Locate every Plasmodium malariae-infected red blood cell.
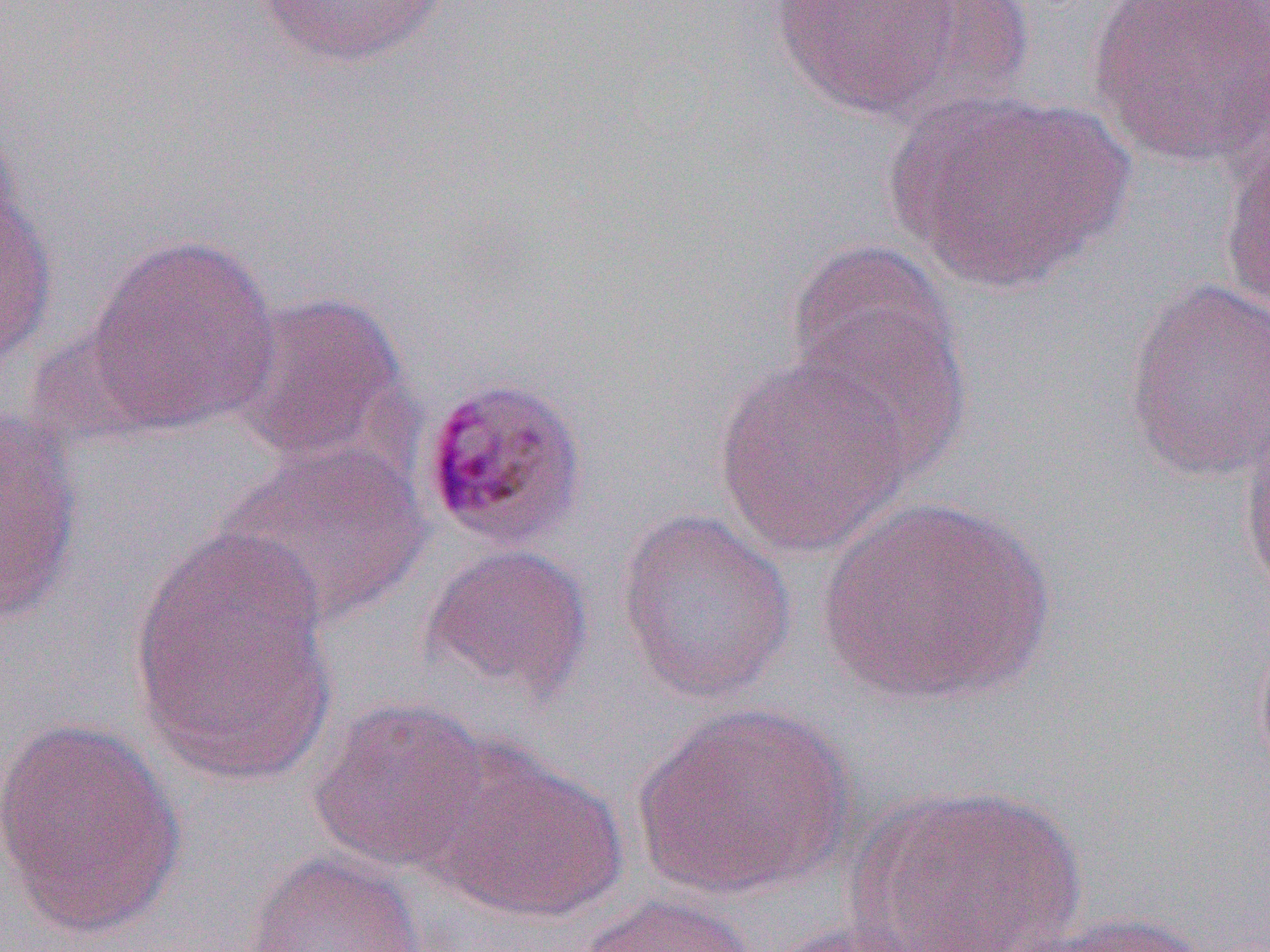
Approximate bounding boxes as named x1/y1/x2/y2 corners in pixels.
Plasmodium malariae-infected red blood cells: (x1=417, y1=375, x2=590, y2=551).

Summary:
  - Uninfected red blood cell locations: (x1=253, y1=0, x2=452, y2=69), (x1=769, y1=0, x2=969, y2=121), (x1=863, y1=0, x2=1037, y2=123), (x1=1086, y1=0, x2=1270, y2=171), (x1=882, y1=87, x2=1131, y2=294), (x1=0, y1=114, x2=23, y2=262), (x1=1219, y1=140, x2=1270, y2=322), (x1=0, y1=190, x2=58, y2=371), (x1=84, y1=232, x2=282, y2=434), (x1=787, y1=253, x2=973, y2=485), (x1=1123, y1=276, x2=1270, y2=487), (x1=228, y1=289, x2=412, y2=467), (x1=713, y1=357, x2=914, y2=560), (x1=0, y1=408, x2=85, y2=627), (x1=1239, y1=411, x2=1270, y2=609), (x1=218, y1=442, x2=430, y2=628), (x1=815, y1=495, x2=1057, y2=707), (x1=615, y1=508, x2=796, y2=706), (x1=127, y1=529, x2=336, y2=787), (x1=420, y1=543, x2=594, y2=701), (x1=1252, y1=623, x2=1270, y2=794), (x1=306, y1=697, x2=495, y2=874), (x1=633, y1=701, x2=853, y2=900), (x1=1, y1=715, x2=187, y2=940), (x1=429, y1=747, x2=629, y2=925), (x1=849, y1=782, x2=1087, y2=952), (x1=246, y1=850, x2=426, y2=951), (x1=573, y1=893, x2=759, y2=952), (x1=1020, y1=911, x2=1214, y2=952), (x1=758, y1=920, x2=930, y2=952)
  - Slide-level diagnosis: Plasmodium malariae
  - Field of view: one of a larger specimen
  - Preparation: thin blood film
  - Image size: 1270×952 pixels
  - Modality: optical microscopy
  - Magnification: 1000x